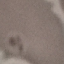
Summary:
  - Malaria status: uninfected
  - Preparation: thin blood smear
  - Capture: smartphone through the microscope eyepiece
  - Stain: Giemsa
  - Image type: cell patch, automatically extracted from a larger field of view and resized to 64 × 64 pixels